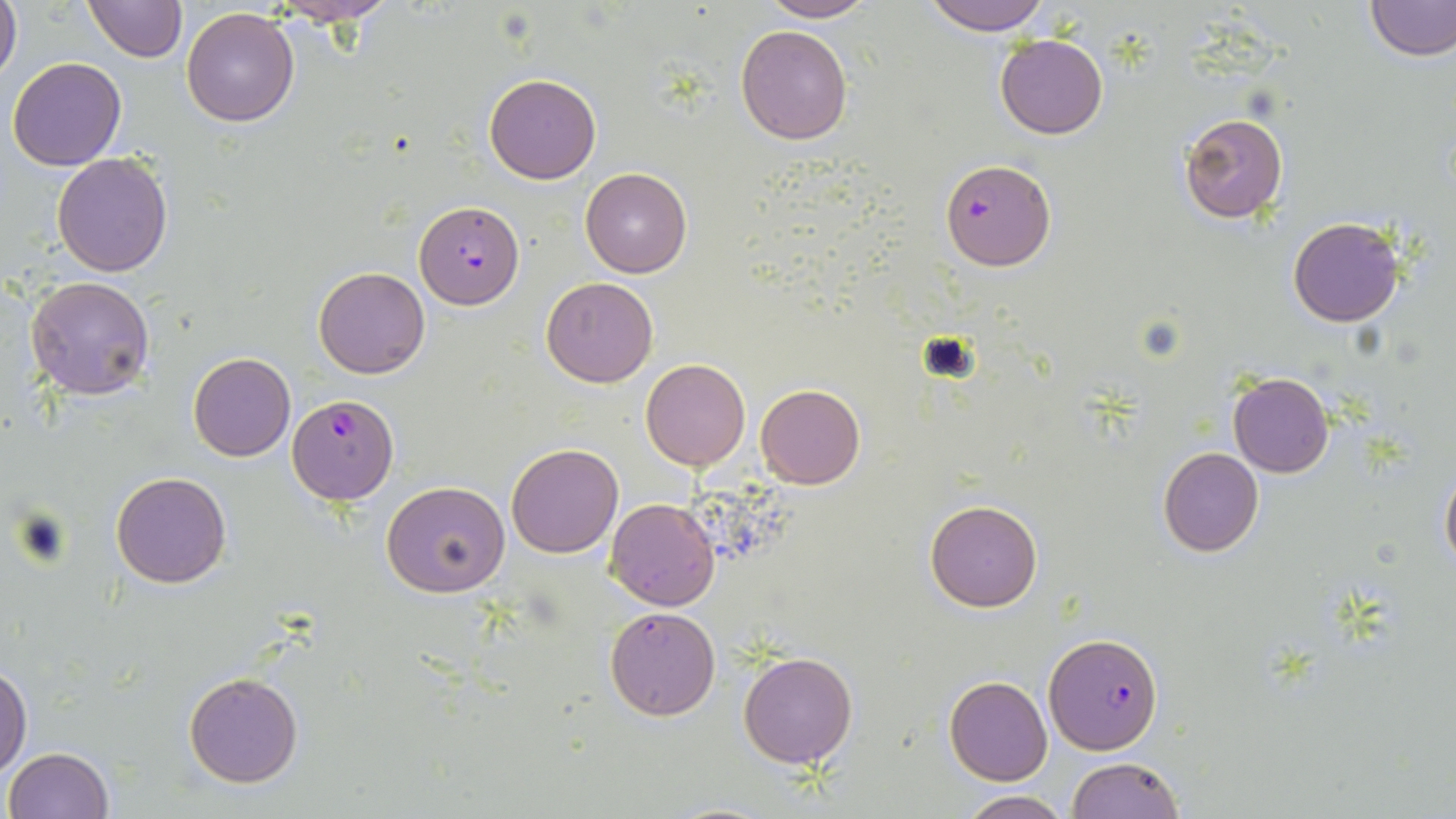
Approximate bounding boxes as (x1,y1)-(x2,y2) corner pairs in pixels. Uninfected red blood cell locations: (0,0)-(23,87), (82,0)-(187,64), (756,0)-(879,22), (923,0)-(1053,36), (1365,0)-(1454,61), (266,2)-(406,26), (181,8)-(300,128), (736,25)-(853,146), (995,34)-(1108,139), (7,56)-(126,171), (483,74)-(601,185), (1178,111)-(1289,224), (53,152)-(174,278), (580,168)-(692,278), (1288,216)-(1404,327), (314,267)-(429,378), (26,275)-(155,400), (541,277)-(658,388), (188,352)-(295,461), (641,358)-(751,470), (1227,373)-(1332,477), (755,382)-(866,489), (506,443)-(623,559), (1158,447)-(1263,557), (1440,461)-(1456,574), (112,471)-(232,589), (382,482)-(510,599), (606,498)-(720,611), (926,500)-(1043,611), (605,606)-(721,721), (738,650)-(858,769), (0,663)-(32,777), (183,671)-(302,788), (944,677)-(1053,785), (4,747)-(114,819), (1066,757)-(1183,819), (957,791)-(1073,818). Plasmodium falciparum-infected red blood cell locations: (940,159)-(1055,271), (415,203)-(524,310), (288,394)-(398,505), (1043,633)-(1164,754). Slide-level diagnosis: Plasmodium falciparum. Thin blood film. May-Grünwald-Giemsa stain. Captured at 1000x magnification. Single field of view. Image is 1456×819 pixels. Optical microscopy.